Identify the blood parasite species.
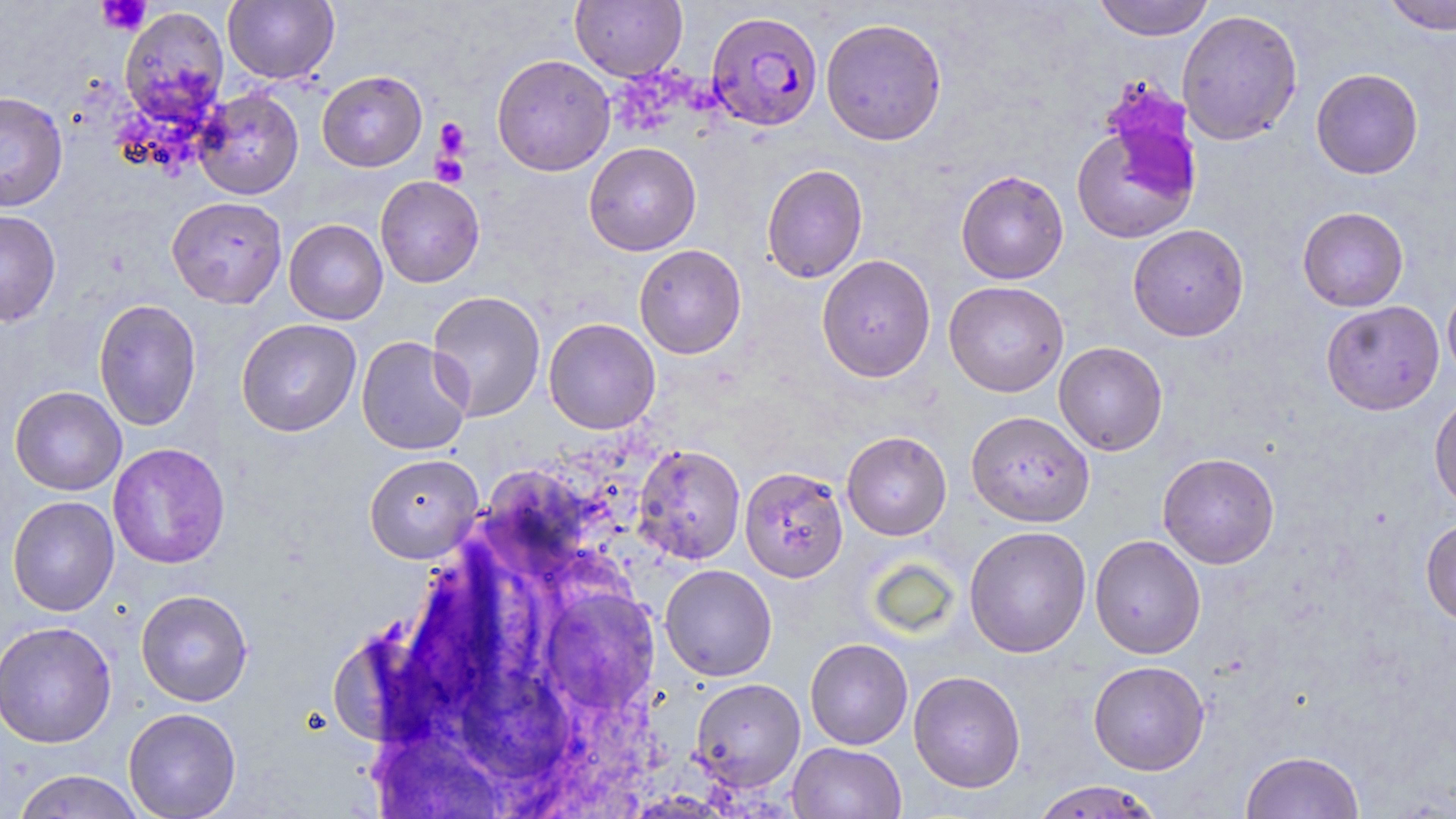
Plasmodium falciparum.

Approximate bounding boxes as (x1, y1, x2, y2) in pixels. Plasmodium falciparum-infected red blood cell locations: (707, 10, 823, 132). Uninfected red blood cell locations: (223, 0, 339, 84), (570, 0, 688, 81), (1092, 0, 1214, 41), (1381, 0, 1456, 35), (119, 6, 229, 127), (1177, 9, 1303, 146), (821, 17, 947, 146), (491, 54, 616, 176), (1310, 68, 1424, 179), (316, 70, 427, 172), (194, 88, 304, 200), (0, 90, 68, 212), (1070, 113, 1201, 245), (584, 142, 701, 256), (761, 163, 868, 283), (955, 170, 1069, 284), (375, 175, 485, 288), (167, 196, 287, 309), (1297, 206, 1409, 312), (0, 209, 61, 327), (284, 219, 388, 325), (1127, 224, 1249, 342), (634, 244, 747, 359), (817, 254, 936, 382), (943, 281, 1069, 397), (1442, 281, 1456, 388), (426, 290, 546, 422), (93, 299, 202, 431), (1321, 300, 1444, 415), (544, 317, 661, 434), (236, 318, 362, 437), (356, 336, 473, 456), (1054, 341, 1168, 456), (10, 386, 127, 496), (1429, 392, 1456, 512), (966, 411, 1095, 527), (841, 431, 952, 540), (107, 443, 231, 569), (632, 443, 746, 565), (1157, 452, 1280, 569), (364, 453, 483, 563), (740, 466, 848, 582), (7, 496, 119, 616), (1421, 520, 1456, 627), (963, 525, 1092, 658), (1090, 535, 1206, 659), (660, 564, 778, 681), (135, 589, 253, 707), (0, 620, 117, 748), (805, 638, 913, 750), (1088, 660, 1210, 775), (908, 670, 1026, 793), (690, 678, 805, 792), (123, 707, 241, 819), (788, 742, 906, 819), (1240, 750, 1365, 819), (11, 769, 146, 818), (1030, 780, 1165, 819). Platelet locations: (97, 0, 152, 35), (434, 118, 470, 160), (431, 154, 468, 187). Optical microscopy. May-Grünwald-Giemsa stain. Thin blood smear. One field of a larger specimen. Image is 1456×819 pixels. 1000x magnification.